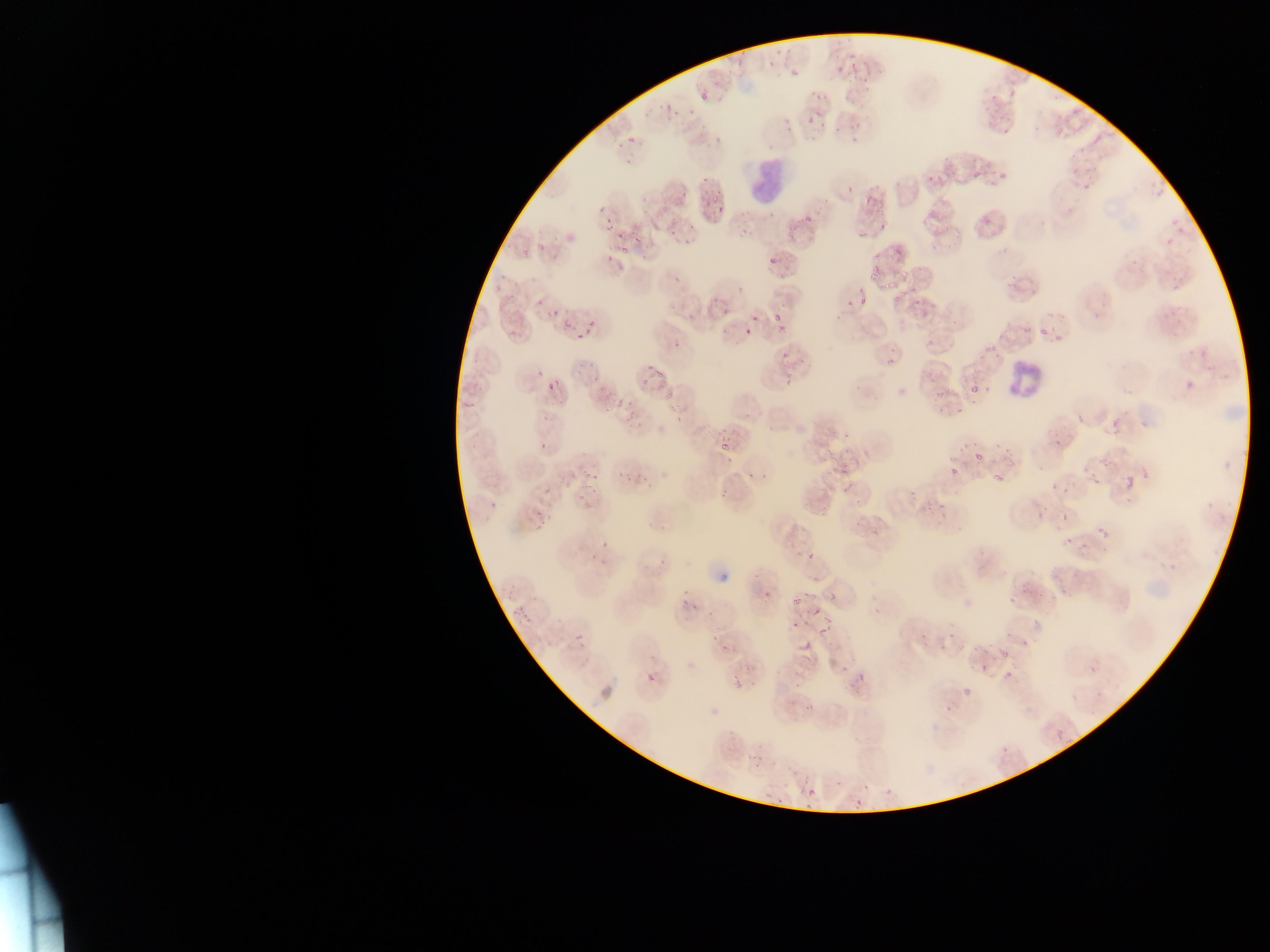

Approximate bounding boxes as [left, top, right, bottom] in pixels.
Summary:
  - Leukocyte locations: [743, 153, 793, 208], [1000, 354, 1050, 407]
  - Plasmodium parasite locations: [846, 51, 855, 61], [768, 60, 777, 67], [838, 65, 846, 72], [791, 67, 802, 77], [853, 67, 861, 74], [861, 75, 872, 86], [862, 86, 870, 96], [700, 92, 711, 101], [815, 106, 824, 119], [806, 117, 814, 129], [854, 119, 865, 130], [832, 127, 843, 134], [850, 133, 864, 144], [627, 135, 638, 146], [972, 171, 982, 179], [997, 171, 1008, 182], [927, 174, 936, 182], [847, 185, 857, 195], [709, 189, 722, 200], [864, 196, 874, 207], [712, 199, 730, 217], [799, 216, 818, 227], [604, 220, 615, 232], [878, 222, 888, 231], [856, 231, 873, 240], [638, 238, 646, 251], [540, 242, 548, 251], [890, 244, 907, 257], [620, 246, 629, 257], [521, 247, 529, 259], [767, 254, 781, 270], [549, 255, 560, 261], [867, 265, 881, 281], [882, 280, 892, 291], [892, 292, 906, 302], [535, 296, 545, 306], [859, 296, 868, 306], [846, 299, 857, 308], [552, 305, 561, 315], [771, 312, 784, 320], [751, 315, 759, 323], [586, 316, 599, 331], [562, 321, 571, 332], [1039, 324, 1053, 338], [507, 327, 520, 339], [744, 328, 754, 336], [577, 334, 587, 342], [674, 339, 686, 346], [925, 339, 935, 349], [884, 355, 898, 369], [650, 364, 656, 376], [656, 364, 667, 377], [534, 370, 546, 378], [586, 373, 599, 385], [1187, 375, 1196, 387], [549, 378, 559, 387], [969, 379, 986, 398], [548, 380, 553, 395], [666, 391, 675, 401], [602, 392, 611, 398], [933, 392, 943, 403], [624, 401, 635, 412], [616, 402, 624, 408], [601, 406, 609, 415], [956, 407, 967, 417], [628, 411, 638, 421], [1076, 415, 1084, 425], [675, 416, 683, 422], [1106, 417, 1117, 430], [1052, 438, 1066, 449], [994, 439, 1006, 448], [540, 441, 547, 450], [719, 441, 731, 449], [823, 446, 838, 464], [976, 447, 986, 464], [1003, 450, 1015, 462], [1098, 458, 1107, 470], [834, 464, 851, 479], [949, 465, 964, 480], [745, 468, 753, 480], [617, 470, 622, 478], [760, 472, 770, 482], [995, 472, 1009, 486], [1091, 474, 1104, 488], [1121, 474, 1139, 493], [594, 476, 603, 483], [541, 477, 549, 496], [1062, 483, 1069, 495], [842, 484, 850, 496], [937, 484, 947, 509], [1050, 485, 1058, 492], [720, 489, 727, 500], [488, 498, 501, 510], [534, 505, 545, 518], [1033, 509, 1048, 520], [1061, 513, 1075, 522], [537, 521, 543, 529], [1094, 523, 1112, 542], [1066, 533, 1075, 544], [808, 548, 820, 560], [749, 571, 761, 579], [765, 585, 775, 598], [1009, 586, 1026, 608], [826, 590, 841, 598], [792, 591, 802, 602], [680, 593, 689, 608], [812, 612, 822, 616], [789, 624, 797, 629], [710, 628, 721, 640], [818, 629, 832, 632], [574, 632, 585, 644], [721, 639, 732, 657], [800, 642, 811, 650], [999, 647, 1012, 661], [834, 658, 845, 673], [980, 658, 991, 673], [1005, 667, 1016, 681], [859, 670, 866, 682], [646, 672, 657, 685], [732, 676, 743, 688], [958, 691, 971, 702], [1053, 728, 1066, 740], [1003, 746, 1013, 751], [807, 787, 817, 798] | approximate [x, y] pixel centers of objects too small to bound: [621, 233], [933, 306]
  - Field of view: single
  - Capture: mobile-phone photograph through a microscope
  - Country: Ghana
  - Image size: 1270×952 pixels
  - Preparation: thin blood smear